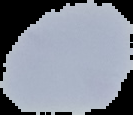
Summary:
  - Image type: cell region segmented out of the field of view; surrounding area masked to black
  - Image size: 133×115 pixels
  - Preparation: thin blood film
  - Result: no malaria parasites detected